State the preparation type.
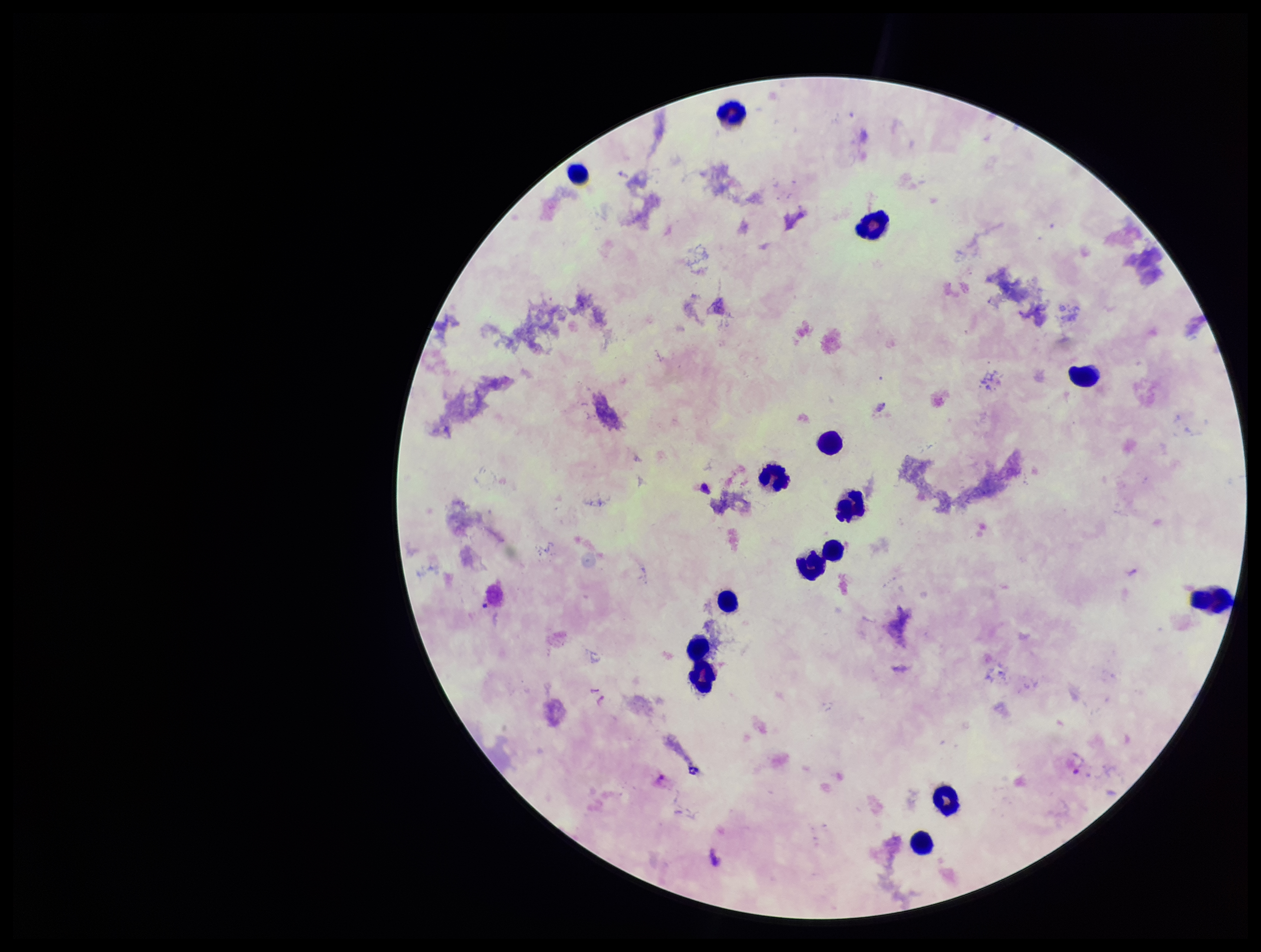
A thick smear.

Image is 1261×952 pixels. Plasmodium parasites: seen. Parasite count: 2. Patient malaria status: positive. Single field of view. Smartphone photograph taken through the eyepiece of a microscope. Leukocyte count: 15. Species reported for this patient: Plasmodium vivax. Stained with Giemsa.